Outline each uninfected red blood cell.
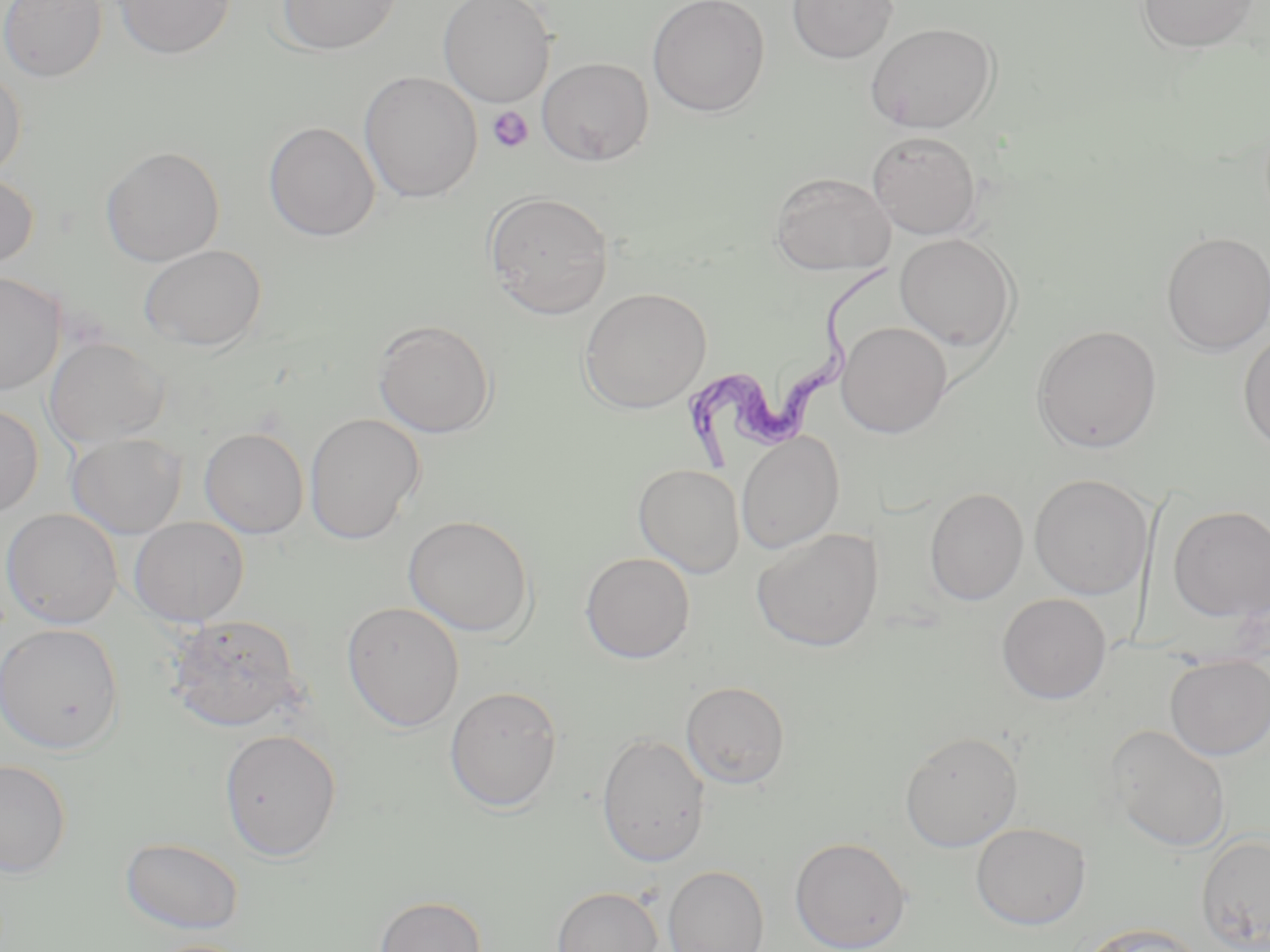
Approximate bounding boxes as [x1, y1, x2, y2] in pixels.
Uninfected red blood cells: [0, 0, 108, 82], [112, 0, 237, 60], [276, 0, 401, 56], [437, 0, 556, 107], [647, 0, 770, 118], [788, 0, 897, 64], [1136, 0, 1260, 54], [865, 22, 999, 133], [537, 57, 654, 166], [0, 66, 27, 181], [359, 71, 483, 203], [263, 121, 380, 241], [867, 130, 982, 239], [100, 145, 224, 266], [0, 171, 38, 270], [770, 172, 895, 275], [483, 191, 615, 319], [1161, 231, 1270, 355], [894, 232, 1019, 351], [140, 244, 266, 351], [0, 271, 66, 395], [579, 287, 712, 413], [373, 319, 496, 438], [836, 321, 952, 437], [1031, 324, 1163, 453], [1238, 330, 1270, 454], [45, 337, 169, 449], [0, 404, 43, 518], [303, 413, 425, 545], [199, 427, 309, 539], [736, 431, 844, 554], [66, 433, 187, 538], [633, 463, 744, 577], [1029, 474, 1152, 600], [925, 487, 1028, 605], [1168, 505, 1270, 621], [1, 508, 123, 629], [403, 514, 536, 637], [129, 517, 250, 627], [751, 528, 883, 652], [580, 551, 695, 663], [997, 593, 1111, 704], [341, 601, 465, 732], [167, 613, 304, 733], [0, 623, 125, 755], [1165, 655, 1270, 759], [681, 681, 790, 788], [444, 685, 563, 812], [1107, 725, 1232, 852], [218, 728, 343, 861], [900, 730, 1023, 851], [596, 732, 711, 867], [0, 759, 72, 879], [970, 822, 1091, 930], [1196, 832, 1270, 951], [120, 836, 244, 935], [789, 836, 912, 952], [663, 865, 770, 952], [552, 885, 663, 952], [374, 895, 487, 952], [1078, 922, 1206, 952], [139, 939, 260, 952].

Platelet locations: [487, 106, 534, 153]. Trypanosoma brucei locations: [678, 261, 899, 473]. Slide-level diagnosis: Trypanosoma brucei. Thin blood film. Image is 1270×952 pixels. May-Grünwald-Giemsa-stained preparation. Single field of view. Optical microscopy. 1000x magnification.